Outline each white blood cell.
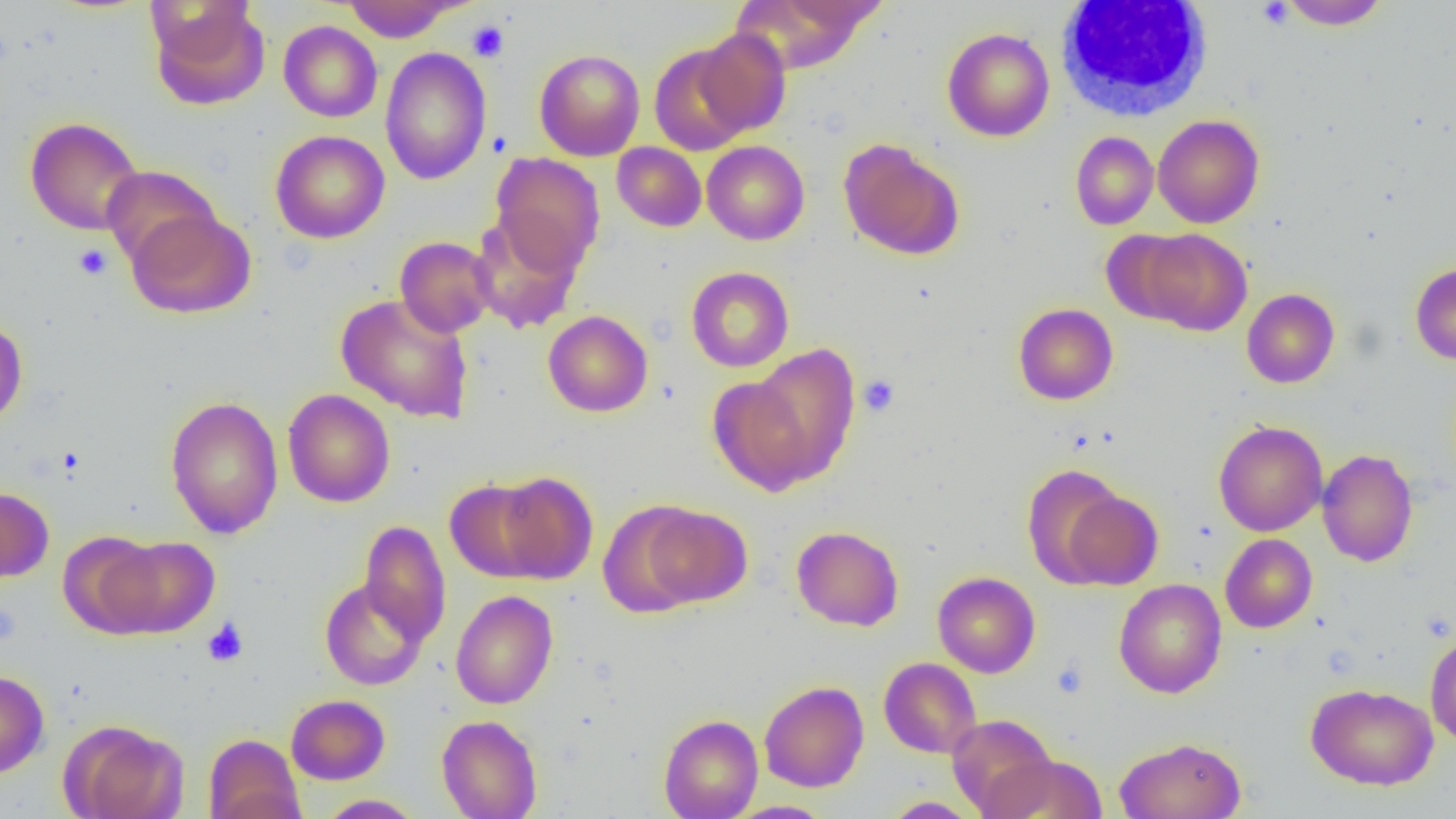

Approximate bounding boxes as named x1/y1/x2/y2 corners in pixels.
White blood cells: (x1=1056, y1=3, x2=1215, y2=120).

slide-level diagnosis = negative for blood parasites
field of view = single
modality = optical microscopy
uninfected red blood cell locations = approximate bounding boxes as named x1/y1/x2/y2 corners in pixels: (x1=733, y1=0, x2=878, y2=74), (x1=1277, y1=0, x2=1391, y2=30), (x1=343, y1=1, x2=462, y2=42), (x1=149, y1=2, x2=270, y2=111), (x1=278, y1=21, x2=382, y2=122), (x1=942, y1=27, x2=1055, y2=142), (x1=694, y1=29, x2=791, y2=137), (x1=650, y1=43, x2=755, y2=155), (x1=379, y1=47, x2=492, y2=185), (x1=534, y1=49, x2=646, y2=161), (x1=1153, y1=115, x2=1264, y2=228), (x1=24, y1=116, x2=144, y2=236), (x1=270, y1=130, x2=390, y2=244), (x1=1070, y1=131, x2=1158, y2=230), (x1=838, y1=139, x2=963, y2=261), (x1=702, y1=140, x2=809, y2=245), (x1=612, y1=142, x2=706, y2=232), (x1=491, y1=153, x2=604, y2=275), (x1=101, y1=165, x2=221, y2=267), (x1=126, y1=208, x2=256, y2=319), (x1=470, y1=212, x2=584, y2=333), (x1=1100, y1=229, x2=1201, y2=326), (x1=1137, y1=229, x2=1252, y2=336), (x1=395, y1=236, x2=497, y2=338), (x1=1410, y1=262, x2=1456, y2=365), (x1=686, y1=266, x2=794, y2=372), (x1=1242, y1=288, x2=1339, y2=388), (x1=335, y1=293, x2=475, y2=424), (x1=1012, y1=303, x2=1118, y2=405), (x1=543, y1=310, x2=653, y2=417), (x1=0, y1=317, x2=28, y2=430), (x1=746, y1=344, x2=862, y2=486), (x1=708, y1=377, x2=815, y2=495), (x1=282, y1=389, x2=395, y2=508), (x1=165, y1=395, x2=283, y2=539), (x1=1213, y1=420, x2=1328, y2=536), (x1=1317, y1=449, x2=1418, y2=567), (x1=1021, y1=464, x2=1131, y2=587), (x1=491, y1=471, x2=598, y2=584), (x1=445, y1=478, x2=550, y2=582), (x1=0, y1=486, x2=54, y2=582), (x1=1058, y1=488, x2=1163, y2=590), (x1=598, y1=501, x2=710, y2=618), (x1=639, y1=503, x2=752, y2=607), (x1=359, y1=520, x2=451, y2=644), (x1=791, y1=525, x2=904, y2=631), (x1=58, y1=530, x2=165, y2=637), (x1=1220, y1=533, x2=1318, y2=633), (x1=103, y1=535, x2=219, y2=638), (x1=933, y1=571, x2=1040, y2=678), (x1=319, y1=578, x2=430, y2=690), (x1=1113, y1=579, x2=1227, y2=698), (x1=450, y1=590, x2=558, y2=709), (x1=1425, y1=632, x2=1456, y2=746), (x1=879, y1=657, x2=981, y2=758), (x1=0, y1=670, x2=49, y2=779), (x1=759, y1=681, x2=869, y2=792), (x1=1306, y1=683, x2=1438, y2=790), (x1=286, y1=694, x2=390, y2=785), (x1=946, y1=713, x2=1058, y2=816), (x1=436, y1=714, x2=543, y2=819), (x1=658, y1=714, x2=763, y2=819), (x1=61, y1=720, x2=188, y2=819), (x1=203, y1=734, x2=306, y2=819), (x1=1114, y1=736, x2=1247, y2=819), (x1=982, y1=753, x2=1108, y2=818), (x1=316, y1=794, x2=424, y2=818), (x1=881, y1=796, x2=981, y2=818), (x1=724, y1=800, x2=835, y2=818)
preparation = thin blood smear
platelet locations = approximate bounding boxes as named x1/y1/x2/y2 corners in pixels: (x1=1255, y1=1, x2=1295, y2=28), (x1=467, y1=20, x2=509, y2=62), (x1=74, y1=243, x2=112, y2=279), (x1=858, y1=375, x2=899, y2=416), (x1=0, y1=603, x2=21, y2=646), (x1=202, y1=619, x2=249, y2=667), (x1=1051, y1=659, x2=1088, y2=699)
image size = 1456×819 pixels
magnification = 1000x